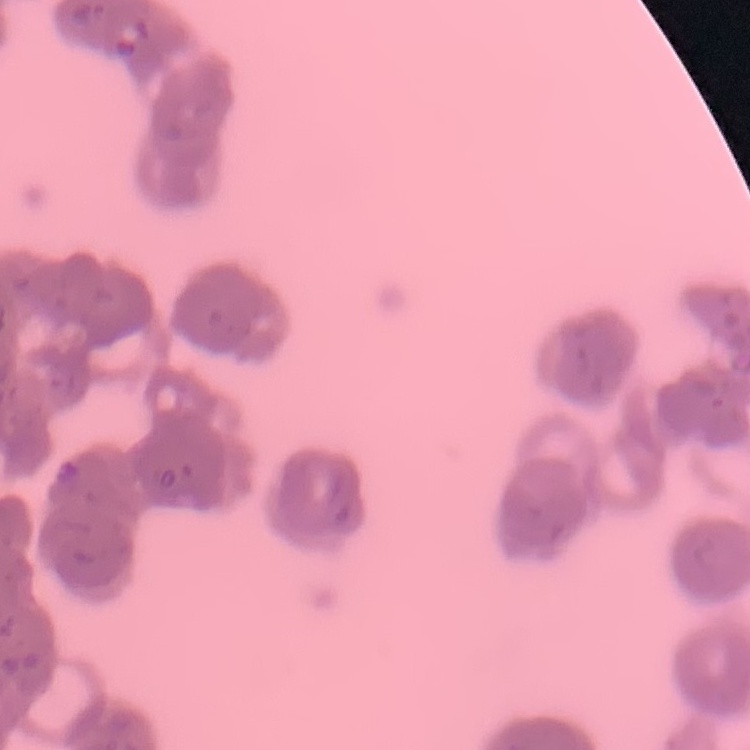

{
  "erythrocyte_morphology": "rouleaux formation",
  "preparation": "thin blood smear",
  "stain": "Field's or Giemsa",
  "image_type": "one tile cut from a larger photomicrograph"
}